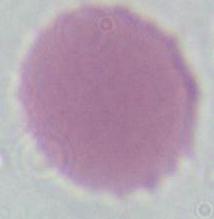
Summary:
  - Magnification: 1000x
  - Modality: micrograph
  - Identification: erythrocyte